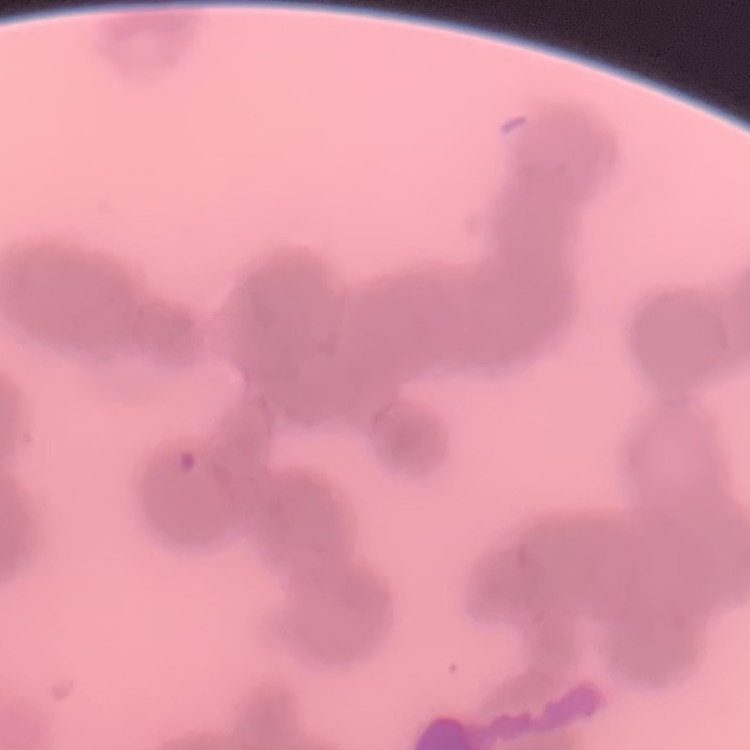

erythrocyte morphology = rouleaux formation
image type = square crop of a larger photomicrograph
preparation = thin peripheral smear
stain = Field's or Giemsa